Assess this cell for malaria.
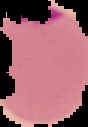

It is parasitized.

From a thin blood film. The area outside the segmented cell region is set to black. Image is 88×127 pixels.